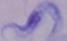
Summary:
  - Identification: trypanosome
  - Modality: micrograph
  - Magnification: 1000x